Describe the morphology of the erythrocytes.
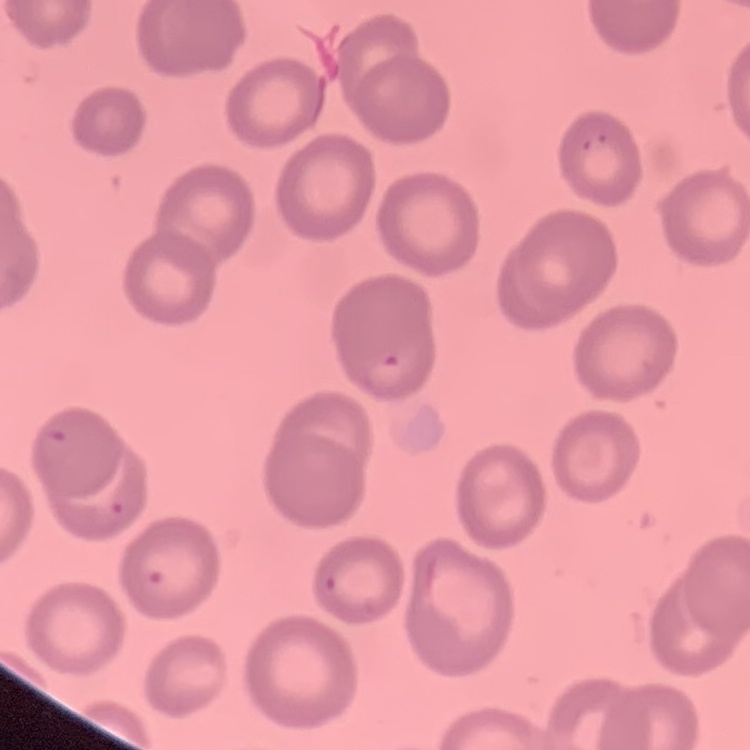
They show no rouleaux formation.

Stained with either Field's or Giemsa. Thin blood film. One tile cut from a larger photomicrograph.